Locate platelets.
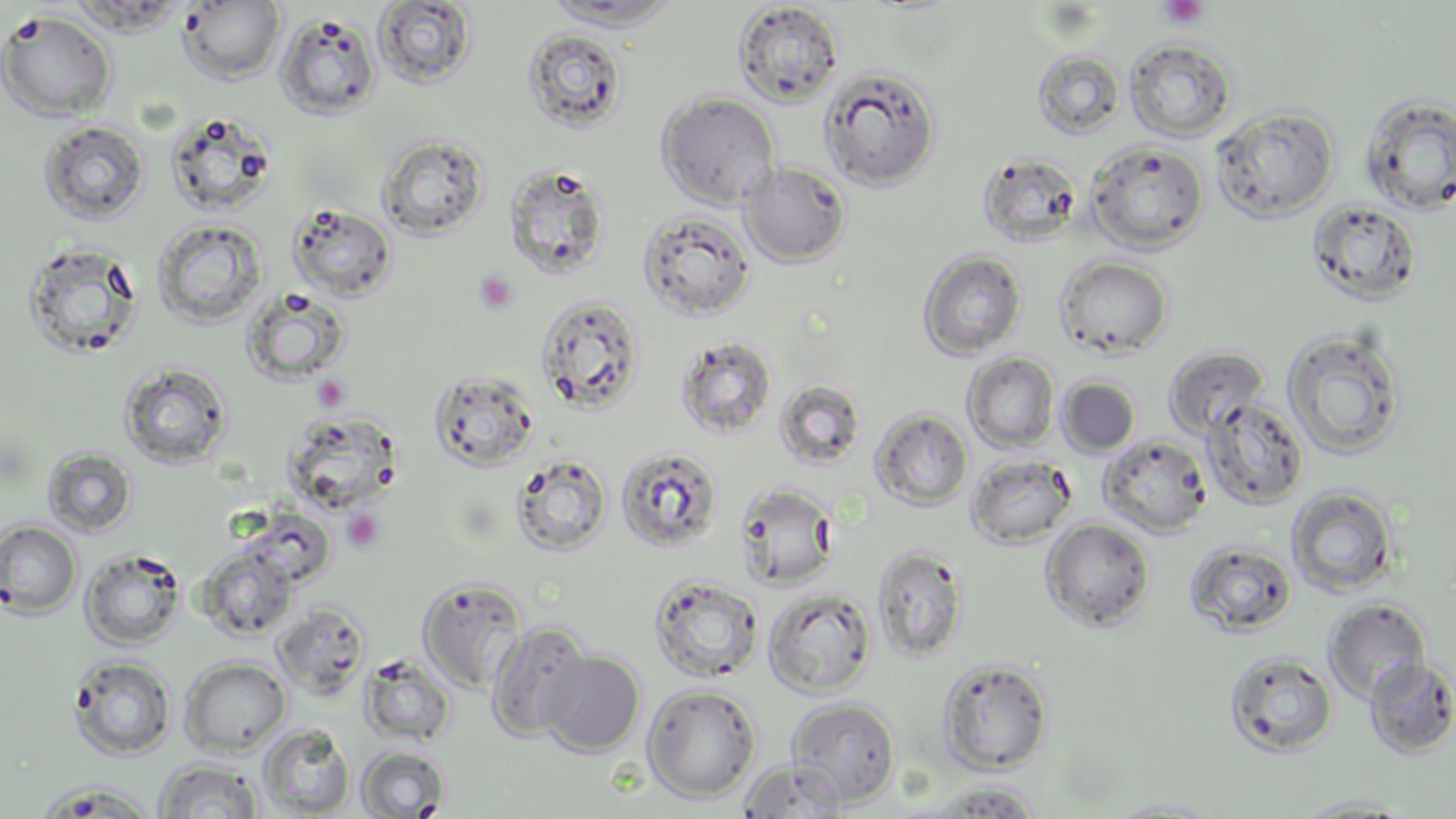

Approximate bounding boxes as named x1/y1/x2/y2 corners in pixels.
Platelets: (x1=1159, y1=0, x2=1209, y2=29), (x1=473, y1=270, x2=519, y2=314), (x1=312, y1=375, x2=350, y2=410), (x1=341, y1=508, x2=384, y2=552).

Summary:
  - Uninfected red blood cell locations: (x1=177, y1=1, x2=286, y2=85), (x1=373, y1=1, x2=478, y2=89), (x1=541, y1=1, x2=685, y2=29), (x1=733, y1=2, x2=844, y2=106), (x1=0, y1=10, x2=117, y2=122), (x1=276, y1=12, x2=382, y2=120), (x1=522, y1=27, x2=628, y2=134), (x1=1124, y1=39, x2=1237, y2=143), (x1=1032, y1=49, x2=1126, y2=140), (x1=819, y1=66, x2=941, y2=189), (x1=657, y1=92, x2=780, y2=209), (x1=1359, y1=95, x2=1456, y2=215), (x1=1211, y1=106, x2=1339, y2=221), (x1=165, y1=110, x2=278, y2=216), (x1=38, y1=120, x2=150, y2=226), (x1=377, y1=133, x2=489, y2=240), (x1=1087, y1=142, x2=1209, y2=253), (x1=977, y1=151, x2=1083, y2=247), (x1=740, y1=161, x2=851, y2=267), (x1=503, y1=162, x2=611, y2=280), (x1=1306, y1=199, x2=1423, y2=305), (x1=288, y1=202, x2=398, y2=302), (x1=639, y1=210, x2=756, y2=321), (x1=151, y1=219, x2=267, y2=329), (x1=22, y1=241, x2=144, y2=360), (x1=918, y1=249, x2=1027, y2=361), (x1=1055, y1=256, x2=1173, y2=358), (x1=242, y1=287, x2=351, y2=386), (x1=535, y1=295, x2=646, y2=415), (x1=1280, y1=327, x2=1407, y2=460), (x1=676, y1=336, x2=778, y2=439), (x1=1163, y1=346, x2=1269, y2=437), (x1=962, y1=352, x2=1060, y2=452), (x1=118, y1=362, x2=233, y2=470), (x1=429, y1=368, x2=540, y2=471), (x1=1058, y1=377, x2=1140, y2=457), (x1=774, y1=379, x2=867, y2=469), (x1=1201, y1=398, x2=1310, y2=511), (x1=871, y1=408, x2=973, y2=511), (x1=281, y1=410, x2=404, y2=515), (x1=1099, y1=433, x2=1212, y2=538), (x1=43, y1=446, x2=137, y2=536), (x1=615, y1=446, x2=724, y2=553), (x1=511, y1=454, x2=613, y2=555), (x1=966, y1=454, x2=1077, y2=549), (x1=734, y1=482, x2=840, y2=590), (x1=1286, y1=486, x2=1400, y2=598), (x1=328, y1=498, x2=389, y2=555), (x1=1040, y1=517, x2=1156, y2=632), (x1=0, y1=520, x2=82, y2=619), (x1=1186, y1=542, x2=1298, y2=637), (x1=873, y1=544, x2=971, y2=664), (x1=81, y1=547, x2=187, y2=649), (x1=196, y1=547, x2=298, y2=641), (x1=649, y1=574, x2=764, y2=683), (x1=418, y1=578, x2=526, y2=691), (x1=763, y1=586, x2=877, y2=698), (x1=1324, y1=598, x2=1431, y2=702), (x1=273, y1=603, x2=370, y2=699), (x1=485, y1=620, x2=593, y2=743), (x1=1224, y1=650, x2=1338, y2=758), (x1=539, y1=651, x2=645, y2=757), (x1=359, y1=653, x2=457, y2=748), (x1=68, y1=655, x2=176, y2=760), (x1=1363, y1=656, x2=1456, y2=758), (x1=180, y1=657, x2=291, y2=755), (x1=936, y1=657, x2=1054, y2=775), (x1=643, y1=684, x2=761, y2=802), (x1=786, y1=697, x2=901, y2=806), (x1=259, y1=725, x2=354, y2=817), (x1=356, y1=746, x2=450, y2=818), (x1=153, y1=758, x2=264, y2=818), (x1=737, y1=760, x2=849, y2=817), (x1=921, y1=780, x2=1046, y2=818), (x1=34, y1=781, x2=160, y2=816), (x1=1293, y1=793, x2=1419, y2=816), (x1=1102, y1=798, x2=1228, y2=817)
  - Slide-level diagnosis: no evidence of blood parasites
  - Modality: optical microscopy
  - Field of view: single
  - Stain: May-Grünwald-Giemsa
  - Magnification: 1000x
  - Preparation: thin blood film
  - Image size: 1456×819 pixels